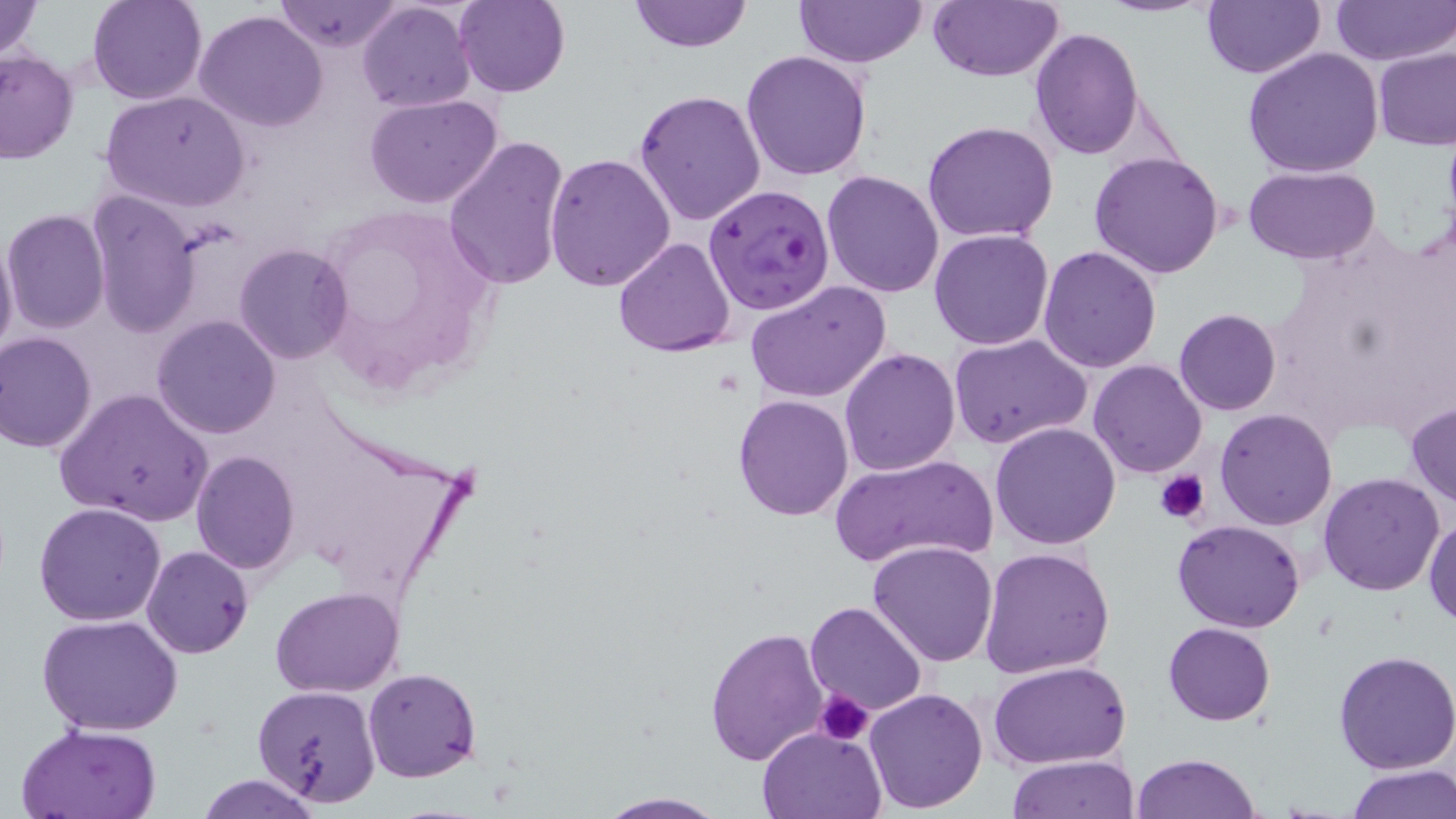
Approximate bounding boxes as [x1, y1, x2, y2] in pixels. Plasmodium falciparum-infected red blood cell locations: [702, 185, 836, 316]. Platelet locations: [1154, 468, 1211, 525], [814, 690, 876, 745]. Uninfected red blood cell locations: [0, 0, 45, 65], [87, 0, 207, 105], [276, 0, 403, 53], [455, 0, 569, 98], [629, 0, 752, 52], [795, 0, 929, 68], [926, 0, 1062, 83], [1096, 0, 1213, 17], [1200, 0, 1326, 80], [1331, 0, 1456, 67], [357, 2, 476, 113], [195, 9, 329, 131], [1030, 27, 1144, 160], [1241, 46, 1386, 177], [1375, 46, 1456, 150], [0, 50, 80, 163], [740, 50, 873, 180], [100, 89, 251, 211], [633, 90, 767, 228], [365, 95, 501, 208], [922, 120, 1060, 244], [443, 134, 570, 291], [545, 151, 676, 292], [1088, 151, 1226, 279], [1242, 166, 1384, 265], [822, 170, 946, 298], [85, 191, 200, 334], [317, 203, 496, 389], [2, 208, 111, 333], [929, 229, 1054, 350], [0, 230, 19, 363], [612, 237, 736, 357], [233, 242, 353, 363], [1038, 245, 1164, 373], [744, 280, 892, 404], [1173, 309, 1282, 415], [152, 315, 281, 439], [0, 331, 99, 452], [949, 332, 1092, 449], [840, 348, 960, 476], [1088, 359, 1209, 477], [52, 388, 213, 527], [733, 394, 853, 520], [1406, 401, 1456, 509], [1215, 408, 1338, 530], [990, 421, 1122, 551], [191, 450, 301, 576], [829, 452, 998, 569], [1316, 471, 1446, 596], [33, 502, 169, 626], [1425, 513, 1456, 628], [1173, 519, 1306, 633], [868, 540, 999, 667], [142, 545, 253, 659], [978, 548, 1116, 679], [270, 586, 405, 696], [804, 601, 928, 717], [38, 613, 184, 736], [1163, 622, 1276, 725], [705, 625, 827, 766], [1333, 650, 1456, 775], [989, 660, 1132, 769], [363, 668, 483, 783], [252, 685, 380, 805], [863, 687, 989, 813], [15, 723, 163, 818], [757, 725, 885, 819], [1131, 752, 1263, 819], [1008, 754, 1139, 818], [1344, 766, 1456, 819], [193, 774, 328, 818], [596, 792, 727, 817]. Slide-level diagnosis: Plasmodium falciparum. One field of a larger specimen. Image is 1456×819 pixels. Optical microscopy. 1000x magnification. Thin blood film. May-Grünwald-Giemsa stain.